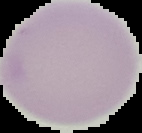

Cell region segmented out of the field of view; the surrounding area is masked to black. From a thin blood smear. Image is 142×133 pixels. Malaria status: uninfected.